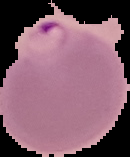
preparation = thin blood smear
result = malaria parasites identified
image type = segmented cell region on a black background
image size = 130×157 pixels